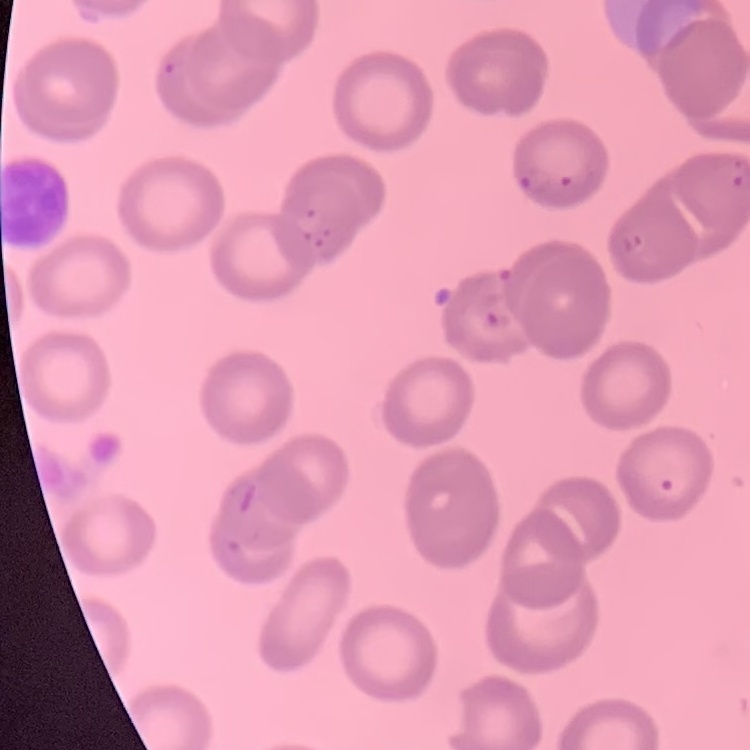

Summary:
  - Erythrocyte morphology: no rouleaux formation
  - Image type: one tile cut from a larger photomicrograph
  - Preparation: thin peripheral smear
  - Stain: Field's or Giemsa